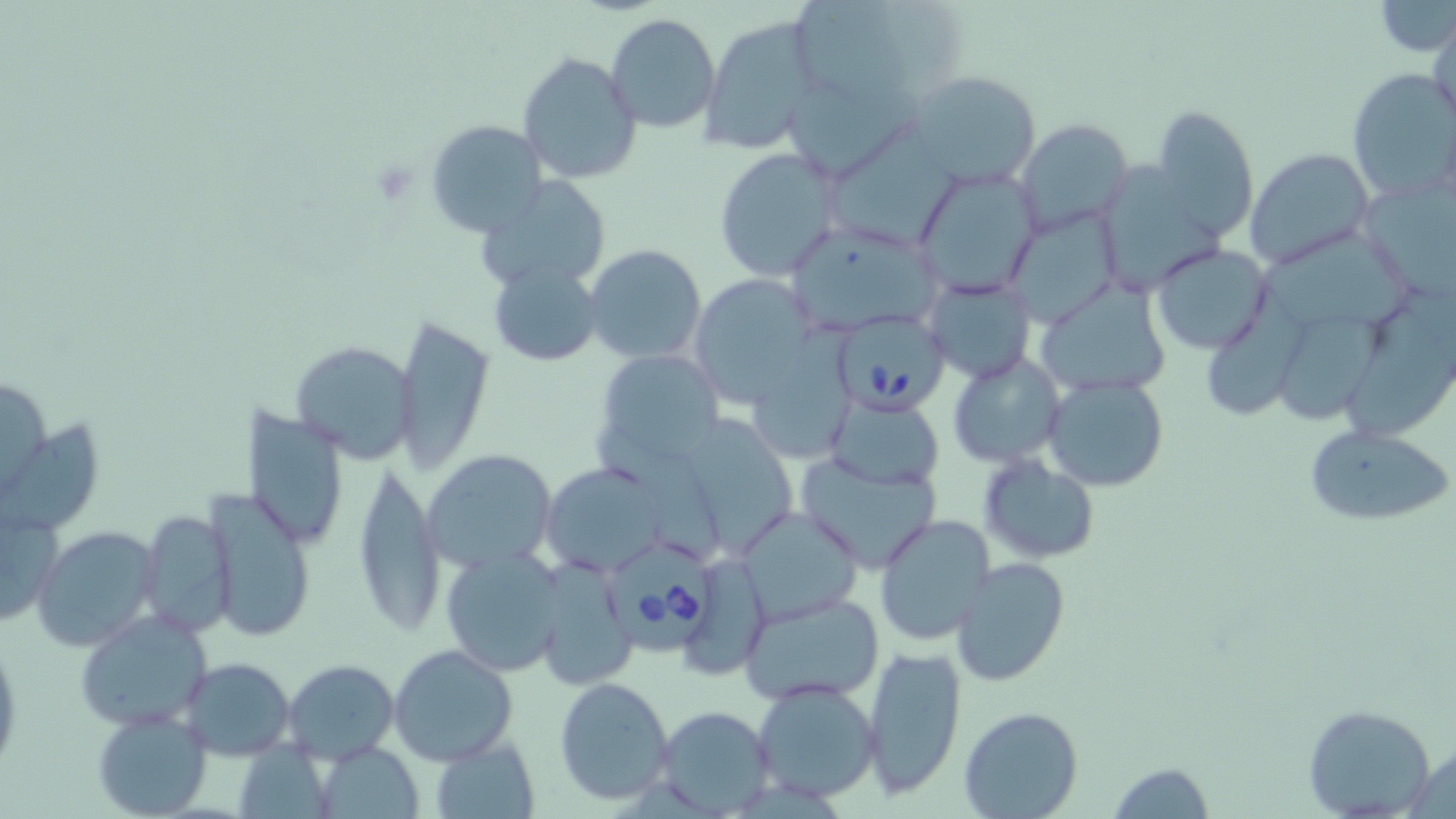

slide_level_diagnosis: Babesia divergens
magnification: 1000x
field_of_view: single
image_size: 1456×819 pixels
platelet_locations: 'approximate bounding boxes as named x1/y1/x2/y2 corners in pixels: (x1=371, y1=159, x2=419, y2=204)'
preparation: thin blood film
stain: May-Grünwald-Giemsa
modality: optical microscopy
uninfected_red_blood_cell_locations: 'approximate bounding boxes as named x1/y1/x2/y2 corners in pixels: (x1=788, y1=0, x2=930, y2=111), (x1=1377, y1=2, x2=1456, y2=55), (x1=607, y1=13, x2=721, y2=133), (x1=699, y1=16, x2=824, y2=153), (x1=1429, y1=18, x2=1456, y2=134), (x1=516, y1=51, x2=641, y2=186), (x1=1346, y1=66, x2=1456, y2=202), (x1=908, y1=70, x2=1040, y2=185), (x1=1152, y1=105, x2=1258, y2=240), (x1=426, y1=119, x2=546, y2=237), (x1=826, y1=121, x2=966, y2=245), (x1=1015, y1=121, x2=1135, y2=237), (x1=711, y1=146, x2=844, y2=282), (x1=1245, y1=148, x2=1376, y2=271), (x1=1101, y1=163, x2=1225, y2=287), (x1=912, y1=165, x2=1043, y2=297), (x1=1360, y1=174, x2=1456, y2=300), (x1=479, y1=176, x2=614, y2=293), (x1=1003, y1=206, x2=1121, y2=327), (x1=789, y1=225, x2=944, y2=328), (x1=1280, y1=228, x2=1414, y2=339), (x1=1151, y1=243, x2=1273, y2=354), (x1=583, y1=244, x2=706, y2=364), (x1=489, y1=257, x2=605, y2=366), (x1=689, y1=273, x2=818, y2=408), (x1=925, y1=273, x2=1034, y2=383), (x1=1032, y1=280, x2=1174, y2=399), (x1=1208, y1=284, x2=1310, y2=422), (x1=1346, y1=297, x2=1456, y2=438), (x1=1278, y1=312, x2=1382, y2=424), (x1=392, y1=315, x2=496, y2=476), (x1=288, y1=338, x2=419, y2=462), (x1=596, y1=349, x2=724, y2=470), (x1=948, y1=353, x2=1066, y2=467), (x1=0, y1=372, x2=49, y2=500), (x1=1044, y1=374, x2=1168, y2=492), (x1=823, y1=396, x2=945, y2=490), (x1=246, y1=408, x2=349, y2=552), (x1=686, y1=413, x2=796, y2=560), (x1=596, y1=423, x2=727, y2=563), (x1=1303, y1=423, x2=1453, y2=527), (x1=422, y1=449, x2=558, y2=571), (x1=795, y1=453, x2=942, y2=572), (x1=978, y1=453, x2=1102, y2=565), (x1=352, y1=461, x2=444, y2=637), (x1=540, y1=461, x2=668, y2=580), (x1=833, y1=479, x2=982, y2=620), (x1=207, y1=488, x2=318, y2=641), (x1=737, y1=506, x2=862, y2=624), (x1=0, y1=507, x2=65, y2=627), (x1=137, y1=509, x2=237, y2=638), (x1=876, y1=514, x2=998, y2=646), (x1=31, y1=525, x2=161, y2=652), (x1=438, y1=547, x2=566, y2=678), (x1=950, y1=557, x2=1070, y2=687), (x1=534, y1=559, x2=636, y2=690), (x1=698, y1=567, x2=771, y2=673), (x1=739, y1=592, x2=885, y2=707), (x1=74, y1=611, x2=214, y2=735), (x1=0, y1=635, x2=22, y2=774), (x1=388, y1=643, x2=519, y2=768), (x1=862, y1=644, x2=968, y2=801), (x1=181, y1=657, x2=296, y2=759), (x1=283, y1=659, x2=399, y2=765), (x1=553, y1=676, x2=675, y2=807), (x1=752, y1=681, x2=882, y2=803), (x1=1303, y1=703, x2=1437, y2=817), (x1=655, y1=706, x2=775, y2=814), (x1=958, y1=707, x2=1084, y2=819), (x1=93, y1=708, x2=213, y2=817), (x1=426, y1=734, x2=541, y2=819), (x1=1403, y1=741, x2=1455, y2=816), (x1=311, y1=742, x2=425, y2=818), (x1=1106, y1=761, x2=1216, y2=817)'
babesia_divergens_infected_red_blood_cell_locations: 'approximate bounding boxes as named x1/y1/x2/y2 corners in pixels: (x1=834, y1=309, x2=948, y2=412), (x1=612, y1=537, x2=716, y2=652)'